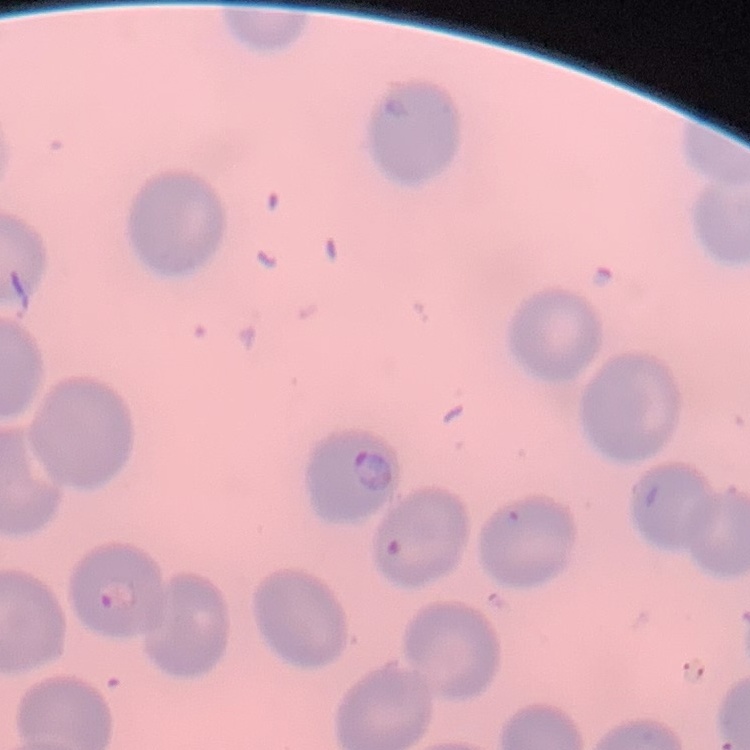
The red blood cells show no rouleaux formation. One tile cut from a larger photomicrograph. Thin peripheral smear. Stained with either Field's or Giemsa.